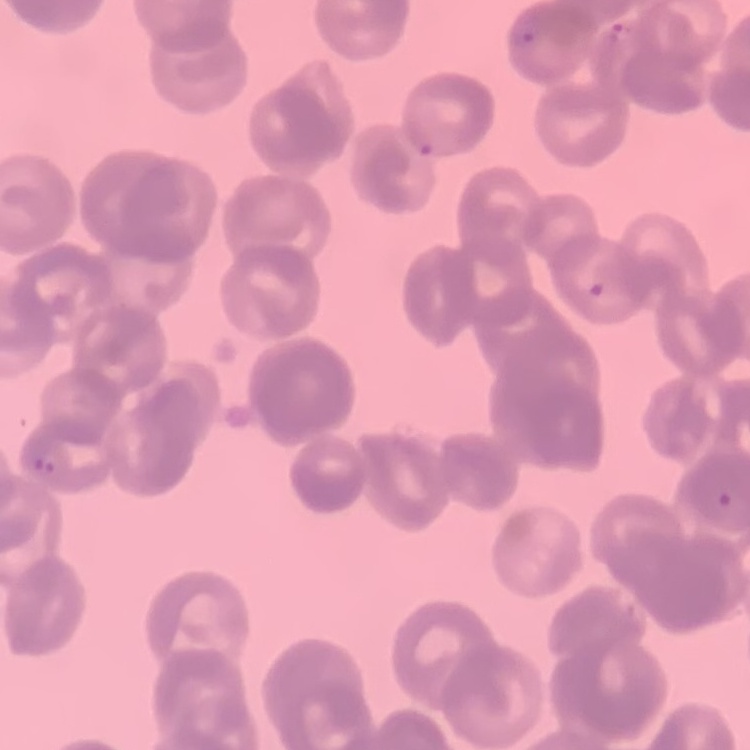

The erythrocytes show rouleaux formation. Square crop of a larger photomicrograph. Thin blood smear. Stained with either Field's or Giemsa.